Locate every uninfected red blood cell.
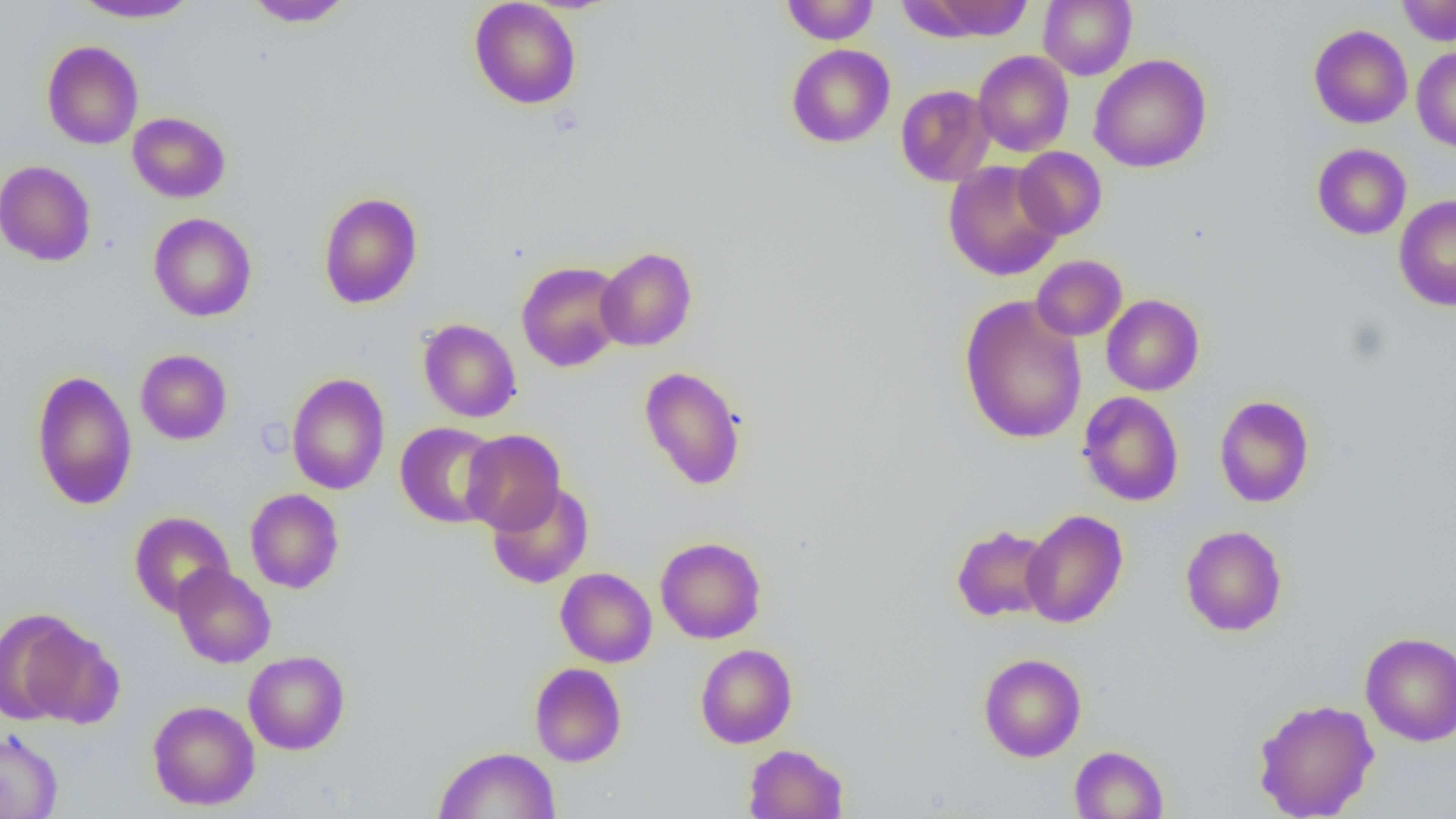

Approximate bounding boxes as named x1/y1/x2/y2 corners in pixels.
Uninfected red blood cells: (x1=71, y1=0, x2=200, y2=23), (x1=244, y1=0, x2=355, y2=28), (x1=469, y1=0, x2=582, y2=109), (x1=781, y1=0, x2=878, y2=44), (x1=906, y1=0, x2=1035, y2=42), (x1=1038, y1=0, x2=1137, y2=80), (x1=1397, y1=0, x2=1456, y2=46), (x1=1309, y1=25, x2=1412, y2=128), (x1=42, y1=41, x2=144, y2=149), (x1=786, y1=44, x2=895, y2=148), (x1=1411, y1=48, x2=1456, y2=152), (x1=973, y1=51, x2=1074, y2=157), (x1=1089, y1=54, x2=1212, y2=173), (x1=896, y1=85, x2=995, y2=186), (x1=127, y1=112, x2=230, y2=203), (x1=1312, y1=143, x2=1411, y2=240), (x1=1014, y1=147, x2=1106, y2=239), (x1=0, y1=160, x2=96, y2=266), (x1=943, y1=160, x2=1063, y2=281), (x1=318, y1=192, x2=422, y2=308), (x1=1394, y1=195, x2=1456, y2=311), (x1=148, y1=213, x2=257, y2=322), (x1=596, y1=247, x2=697, y2=351), (x1=1032, y1=255, x2=1127, y2=341), (x1=516, y1=261, x2=627, y2=372), (x1=1101, y1=294, x2=1204, y2=396), (x1=958, y1=295, x2=1087, y2=445), (x1=418, y1=318, x2=521, y2=423), (x1=135, y1=349, x2=232, y2=444), (x1=639, y1=365, x2=747, y2=490), (x1=30, y1=369, x2=137, y2=510), (x1=286, y1=373, x2=390, y2=495), (x1=1078, y1=391, x2=1184, y2=506), (x1=1214, y1=395, x2=1314, y2=508), (x1=395, y1=422, x2=501, y2=528), (x1=461, y1=429, x2=566, y2=534), (x1=487, y1=481, x2=594, y2=589), (x1=245, y1=488, x2=344, y2=594), (x1=1022, y1=509, x2=1128, y2=628), (x1=129, y1=511, x2=234, y2=616), (x1=951, y1=524, x2=1055, y2=622), (x1=1180, y1=525, x2=1288, y2=636), (x1=655, y1=537, x2=766, y2=644), (x1=171, y1=564, x2=276, y2=669), (x1=555, y1=568, x2=657, y2=667), (x1=0, y1=609, x2=110, y2=725), (x1=1360, y1=632, x2=1456, y2=746), (x1=695, y1=644, x2=797, y2=748), (x1=243, y1=650, x2=350, y2=755), (x1=978, y1=653, x2=1086, y2=762), (x1=529, y1=662, x2=626, y2=767), (x1=1252, y1=698, x2=1380, y2=818), (x1=147, y1=700, x2=260, y2=810), (x1=0, y1=730, x2=62, y2=819), (x1=743, y1=744, x2=848, y2=819), (x1=1069, y1=745, x2=1168, y2=818), (x1=433, y1=746, x2=561, y2=819).

slide-level diagnosis = no evidence of blood parasites
modality = optical microscopy
magnification = 1000x
preparation = thin blood smear
image size = 1456×819 pixels
field of view = one of a larger specimen